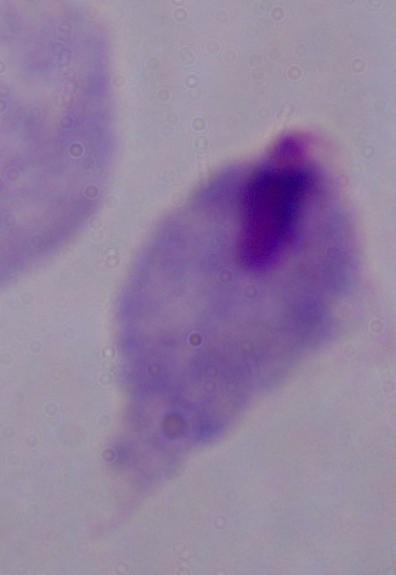
Summary:
  - Magnification: 1000x
  - Identification: trichomonad
  - Modality: photomicrograph